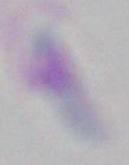

Photomicrograph. Captured at 1000x magnification. Toxoplasma gondii is seen.